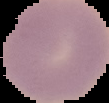

Image is 109×103 pixels. Cell region segmented out of the field of view; the surrounding area is masked to black. Result: negative for Plasmodium parasites. From a thin blood smear.